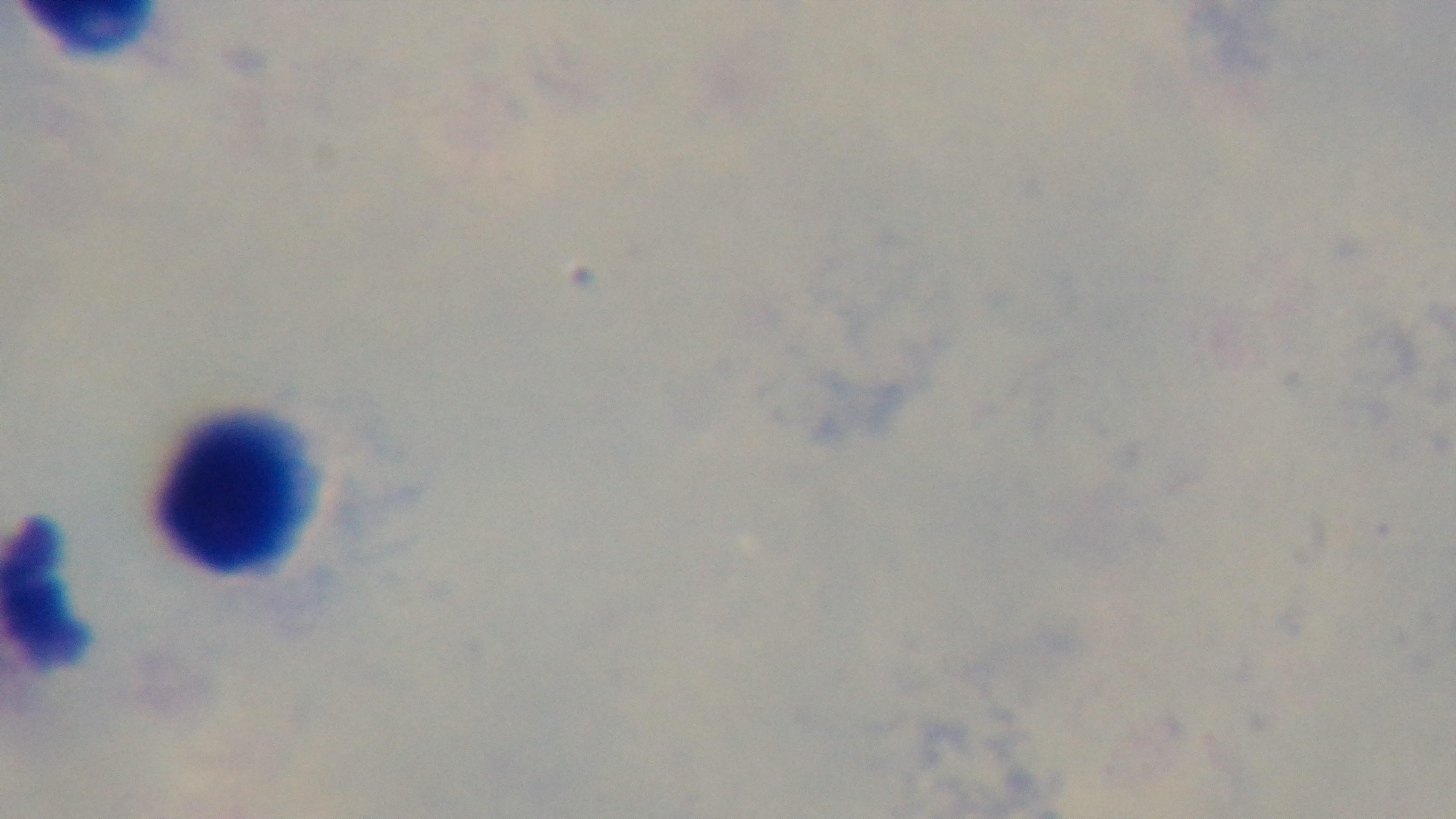 Malaria status: uninfected. 100x oil-immersion objective. Captured with a mounted 4K digital camera. Single field of view. Preparation: thick smear. Giemsa stain. Photomicrograph.